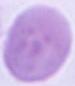

An erythrocyte is shown. 1000x magnification. Photomicrograph.